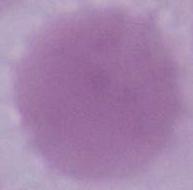

identification = red blood cell
magnification = 1000x
modality = micrograph